Locate every Plasmodium ovale-infected red blood cell.
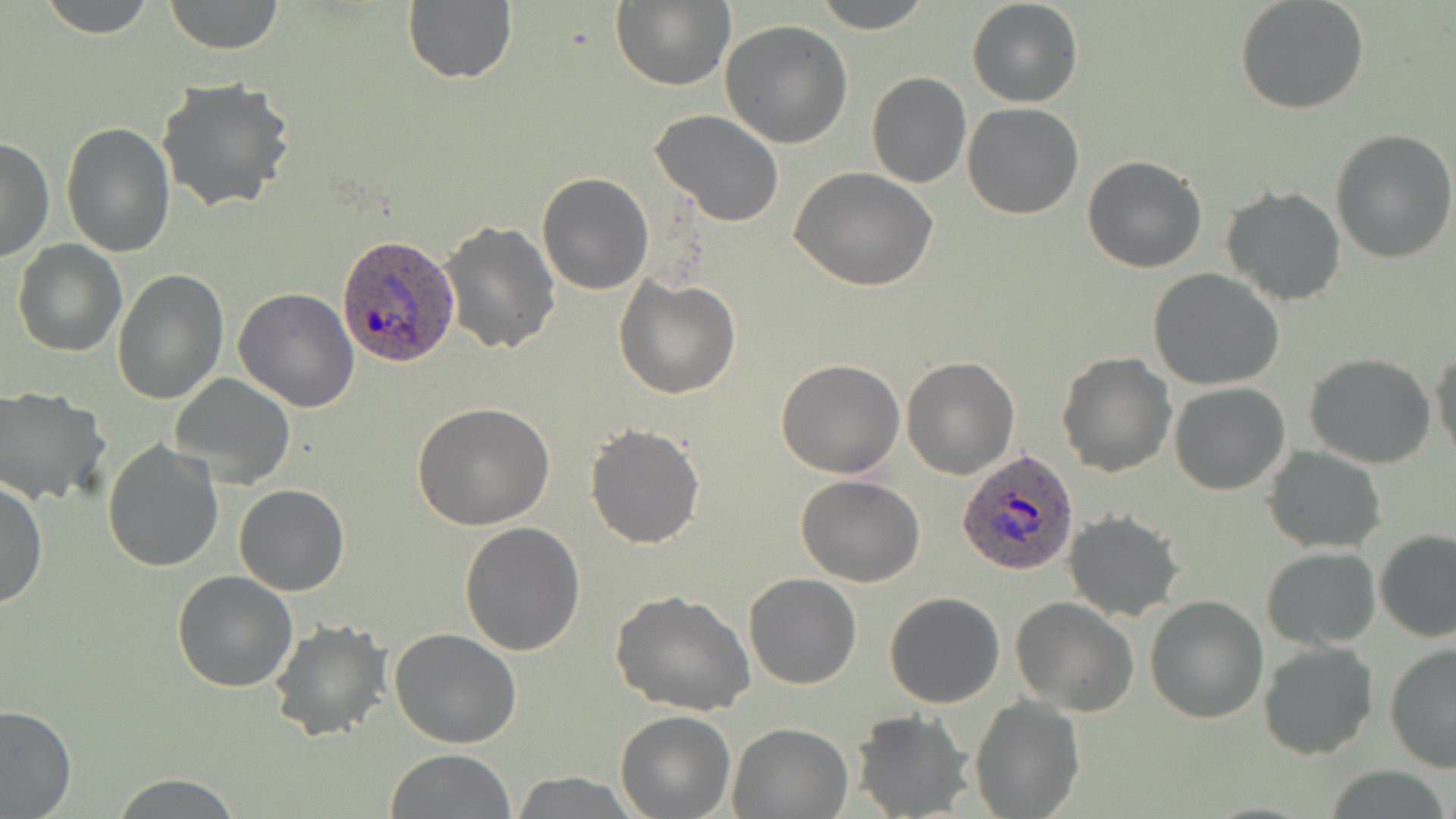
Approximate bounding boxes as (x1,y1)-(x2,y2) corner pairs in pixels.
Plasmodium ovale-infected red blood cells: (337,232)-(461,370), (955,448)-(1080,579).

Uninfected red blood cell locations: (36,0)-(158,37), (164,0)-(284,54), (812,0)-(932,32), (966,0)-(1084,108), (1235,0)-(1370,115), (610,1)-(735,89), (402,2)-(517,84), (719,18)-(852,149), (866,71)-(971,188), (156,77)-(296,214), (962,102)-(1085,219), (650,109)-(785,227), (61,121)-(174,256), (1329,130)-(1456,264), (0,137)-(53,264), (1083,155)-(1206,273), (790,167)-(939,293), (537,172)-(653,294), (1220,186)-(1347,307), (439,220)-(560,355), (11,238)-(126,356), (113,268)-(229,408), (1148,268)-(1284,390), (613,276)-(741,399), (233,288)-(359,412), (1430,347)-(1455,464), (1057,353)-(1177,477), (1304,353)-(1436,469), (902,355)-(1019,478), (776,358)-(906,478), (170,373)-(296,489), (1169,382)-(1290,495), (0,386)-(108,506), (411,403)-(556,532), (585,424)-(705,549), (102,438)-(226,574), (1263,447)-(1387,553), (796,475)-(925,587), (0,478)-(47,609), (233,484)-(349,596), (1063,511)-(1184,622), (458,521)-(586,655), (1375,528)-(1455,642), (1261,545)-(1381,650), (171,570)-(299,693), (743,573)-(862,690), (610,591)-(756,716), (884,591)-(1005,708), (1145,595)-(1269,722), (1012,597)-(1139,716), (267,617)-(393,741), (390,629)-(522,748), (1258,640)-(1378,760), (1385,644)-(1456,775), (970,696)-(1083,819), (0,704)-(75,818), (852,710)-(975,819), (615,711)-(737,818), (728,721)-(852,817), (386,749)-(513,818), (1321,767)-(1455,819), (108,772)-(241,817), (510,773)-(636,817). Slide-level diagnosis: Plasmodium ovale. 1000x magnification. Optical microscopy. Single field of view. Thin blood film. May-Grünwald-Giemsa-stained preparation. Image is 1456×819 pixels.